Locate every blood parasite and identify its species.
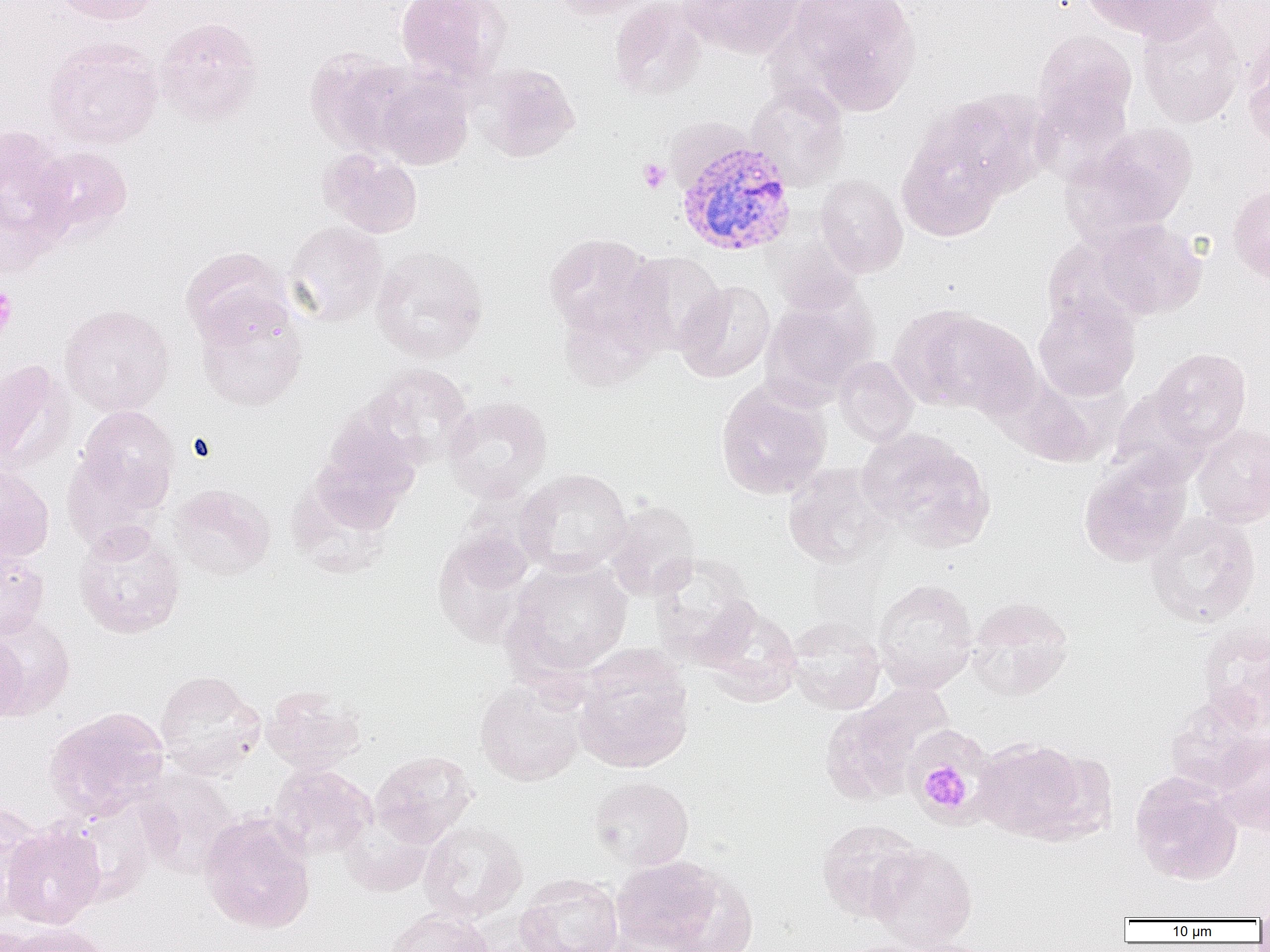
Approximate bounding boxes as (x1,y1)-(x2,y2) corner pairs in pixels.
Plasmodium vivax-infected red blood cells: (675,137)-(797,257).
No Plasmodium falciparum, Plasmodium ovale, Plasmodium malariae, Babesia divergens, or Trypanosoma brucei observed.

slide-level diagnosis = Plasmodium vivax
preparation = thin blood smear
uninfected red blood cell locations = approximate bounding boxes as (x1,y1)-(x2,y2) corner pairs in pixels: (51,0)-(166,25), (395,0)-(512,84), (551,0)-(657,21), (680,0)-(808,59), (787,0)-(921,114), (1081,0)-(1218,43), (608,1)-(708,101), (1137,8)-(1245,128), (154,17)-(264,126), (1033,29)-(1137,138), (43,37)-(163,149), (1242,41)-(1270,153), (305,48)-(421,156), (473,63)-(581,162), (371,68)-(475,169), (746,80)-(850,191), (919,91)-(1045,206), (1068,122)-(1198,238), (0,125)-(74,252), (897,126)-(1008,242), (31,145)-(133,243), (319,147)-(423,238), (815,174)-(908,277), (1228,183)-(1270,286), (1092,219)-(1206,320), (283,221)-(389,326), (542,233)-(662,342), (773,235)-(864,319), (370,246)-(489,363), (181,247)-(292,347), (622,251)-(726,355), (674,280)-(776,382), (762,294)-(876,400), (1033,295)-(1141,401), (59,303)-(175,417), (196,303)-(308,411), (889,304)-(1022,414), (1151,348)-(1251,450), (834,356)-(919,447), (0,359)-(74,475), (361,363)-(476,469), (995,372)-(1115,468), (716,381)-(831,500), (1108,388)-(1212,486), (443,396)-(552,502), (75,406)-(179,514), (313,415)-(423,526), (1191,424)-(1270,527), (860,429)-(995,552), (61,446)-(166,550), (1079,452)-(1193,566), (0,463)-(54,564), (783,463)-(892,569), (516,469)-(632,576), (169,484)-(275,580), (603,500)-(700,600), (1145,511)-(1262,627), (73,521)-(185,639), (432,529)-(536,648), (0,548)-(49,643), (649,554)-(760,667), (504,557)-(633,680), (872,578)-(979,694), (966,597)-(1075,701), (700,601)-(803,705), (0,613)-(75,719), (785,618)-(886,714), (1200,621)-(1270,732), (0,633)-(26,724), (573,651)-(694,774), (154,670)-(265,779), (474,677)-(588,786), (262,685)-(366,773), (821,687)-(949,805), (1164,693)-(1269,794), (43,706)-(171,821), (904,727)-(996,827), (1212,733)-(1270,836), (973,737)-(1089,842), (370,750)-(476,848), (269,763)-(377,861), (136,767)-(241,878), (1130,773)-(1243,885), (588,776)-(693,871), (0,801)-(48,915), (199,813)-(315,933), (340,819)-(434,897), (816,819)-(926,922), (419,821)-(528,923), (2,822)-(105,928), (867,843)-(978,951), (611,855)-(722,951), (660,870)-(758,952), (515,874)-(624,952), (384,907)-(495,952), (5,923)-(114,952), (828,938)-(949,952)
field of view = one of a larger specimen
magnification = 1000x
modality = light microscopy
image size = 1270×952 pixels
platelet locations = approximate bounding boxes as (x1,y1)-(x2,y2) corner pairs in pixels: (637,158)-(671,194), (0,286)-(17,340), (925,768)-(970,808)